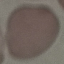
Result: no malaria parasites detected. Giemsa stain. Acquired by smartphone through the microscope eyepiece. Thin blood film. Automatically extracted cell patch, resized to 64 × 64 pixels.